Identify the blood parasite species.
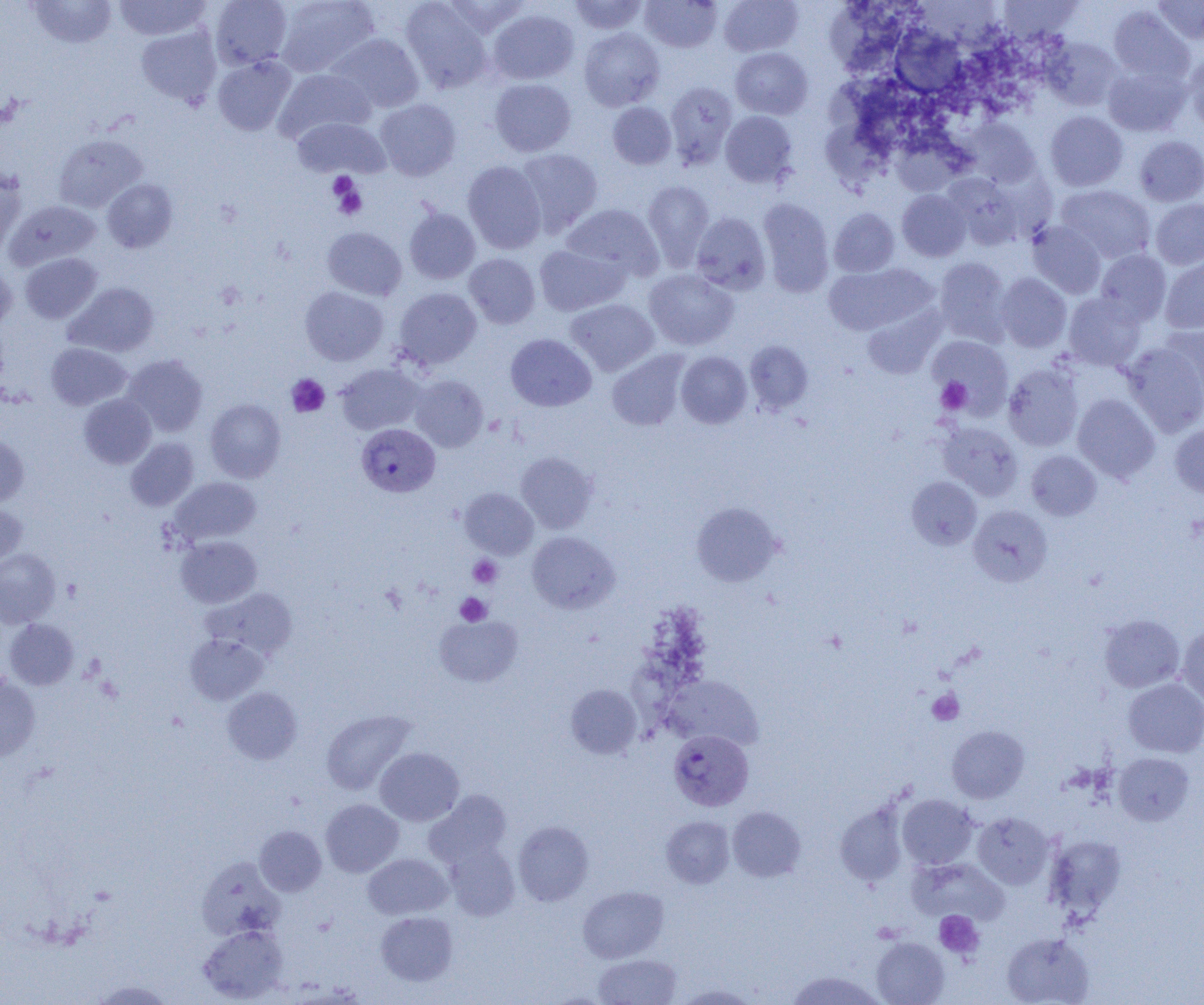

Plasmodium vivax.

uninfected red blood cell locations = approximate bounding boxes as (x1, y1, x2, y2) in pixels: (27, 0, 117, 49), (113, 0, 212, 40), (210, 0, 293, 69), (276, 0, 380, 77), (442, 0, 532, 37), (568, 0, 649, 34), (640, 0, 722, 52), (719, 0, 802, 56), (910, 0, 1007, 57), (998, 0, 1084, 44), (1151, 0, 1204, 44), (400, 1, 494, 93), (826, 4, 904, 75), (1108, 6, 1194, 85), (488, 9, 579, 85), (136, 25, 221, 108), (892, 26, 966, 99), (579, 27, 665, 111), (328, 33, 425, 114), (1043, 37, 1123, 110), (730, 47, 813, 120), (1184, 50, 1204, 132), (212, 56, 297, 136), (1102, 63, 1190, 137), (274, 68, 375, 144), (823, 72, 924, 139), (489, 78, 576, 157), (665, 82, 737, 168), (376, 99, 461, 181), (608, 102, 676, 169), (720, 111, 798, 188), (1045, 111, 1128, 191), (292, 116, 390, 179), (964, 118, 1041, 188), (818, 123, 900, 183), (54, 135, 147, 213), (1134, 135, 1204, 206), (896, 138, 968, 194), (516, 148, 603, 235), (463, 160, 546, 253), (0, 166, 26, 255), (942, 173, 1026, 249), (102, 179, 177, 253), (642, 180, 714, 270), (1057, 185, 1155, 263), (897, 190, 970, 261), (757, 197, 834, 296), (1150, 199, 1204, 269), (5, 200, 101, 270), (562, 204, 663, 281), (829, 207, 899, 277), (404, 208, 480, 284), (691, 212, 771, 294), (1027, 221, 1106, 298), (322, 227, 407, 300), (534, 244, 628, 316), (1095, 249, 1171, 326), (20, 253, 102, 323), (464, 253, 540, 328), (1160, 255, 1204, 333), (934, 257, 1011, 343), (0, 261, 17, 333), (823, 263, 935, 335), (644, 269, 739, 350), (996, 273, 1071, 352), (64, 282, 159, 357), (300, 286, 388, 365), (393, 287, 482, 369), (1063, 293, 1146, 371), (566, 299, 659, 375), (861, 305, 945, 378), (1158, 324, 1204, 400), (505, 334, 596, 411), (928, 336, 1013, 416), (745, 341, 813, 414), (1121, 342, 1204, 436), (46, 343, 132, 410), (607, 351, 690, 431), (676, 352, 752, 428), (123, 354, 208, 437), (336, 363, 424, 435), (1003, 363, 1084, 451), (409, 375, 488, 452), (79, 394, 156, 468), (1073, 394, 1160, 482), (205, 399, 285, 482), (938, 422, 1023, 501), (1170, 423, 1204, 498), (0, 433, 29, 507), (125, 437, 199, 511), (1026, 450, 1101, 520), (516, 451, 598, 533), (907, 476, 982, 550), (170, 477, 261, 545), (460, 488, 538, 559), (0, 502, 28, 566), (691, 502, 782, 586), (968, 505, 1053, 587), (527, 531, 619, 613), (176, 536, 261, 608), (0, 548, 60, 628), (202, 587, 299, 660), (1099, 614, 1184, 692), (435, 615, 522, 687), (4, 619, 79, 690), (1177, 624, 1204, 708), (184, 634, 268, 705), (0, 675, 41, 761), (662, 675, 764, 750), (1123, 678, 1204, 757), (566, 684, 642, 759), (222, 687, 302, 764), (321, 709, 416, 795), (947, 725, 1029, 803), (375, 747, 464, 826), (1114, 753, 1194, 825), (424, 790, 511, 868), (897, 794, 978, 869), (321, 799, 403, 877), (834, 800, 909, 887), (727, 806, 805, 882), (973, 812, 1054, 889), (661, 816, 734, 888), (513, 821, 594, 906), (255, 826, 326, 896), (1045, 834, 1126, 918), (444, 842, 520, 921), (363, 853, 452, 919), (197, 858, 285, 940), (907, 858, 1010, 925), (578, 886, 669, 963), (376, 911, 458, 986), (198, 925, 287, 1003), (1002, 932, 1094, 1005), (872, 937, 949, 1005), (593, 953, 682, 1004), (785, 971, 885, 1004), (91, 979, 174, 1004), (674, 983, 761, 1004)
image size = 1204×1005 pixels
preparation = thin blood smear
Plasmodium vivax-infected red blood cell locations = approximate bounding boxes as (x1, y1, x2, y2) in pixels: (357, 423, 440, 497), (669, 729, 754, 811)
platelet locations = approximate bounding boxes as (x1, y1, x2, y2) in pixels: (328, 171, 359, 202), (329, 176, 367, 220), (286, 374, 330, 417), (936, 377, 971, 414), (468, 555, 502, 588), (455, 592, 491, 626), (927, 689, 964, 724), (934, 910, 984, 959)
magnification = 1000x
field of view = single
modality = optical microscopy